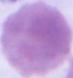

1000x magnification. Photomicrograph. A red blood cell is seen.